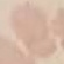
Result: no malaria parasites seen. Photographed with a smartphone camera at the microscope eyepiece. Giemsa stain. Cell patch, automatically extracted from a larger field of view and resized to 64 × 64 pixels. Thin blood film.